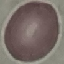 Result: no malaria parasites seen. Thin blood film. Giemsa stain. Automatically extracted cell patch, resized to 64 × 64 pixels. Acquired by smartphone through the microscope eyepiece.